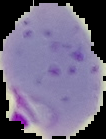

Summary:
  - Preparation: thin blood smear
  - Image type: segmented cell region on a black background
  - Image size: 106×139 pixels
  - Malaria status: parasitized